State the blood parasite species.
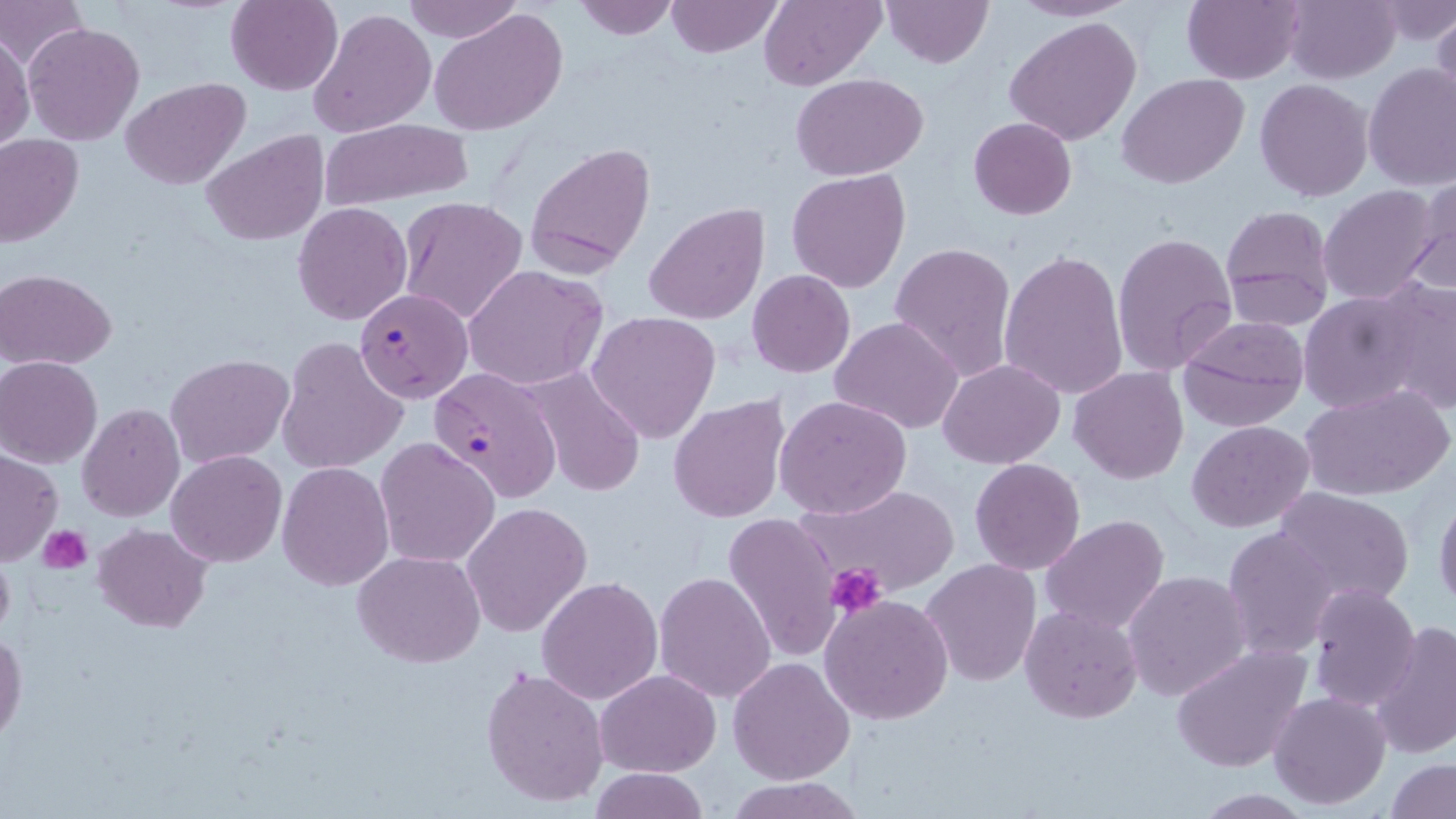

Plasmodium falciparum.

Approximate bounding boxes as (x1, y1, x2, y2) in pixels. Uninfected red blood cell locations: (1, 0, 86, 68), (226, 0, 343, 95), (402, 0, 523, 46), (572, 0, 679, 41), (665, 0, 782, 56), (758, 0, 884, 89), (881, 0, 994, 67), (1010, 0, 1139, 22), (1182, 0, 1305, 85), (1284, 0, 1400, 84), (1379, 1, 1455, 46), (308, 7, 437, 138), (431, 9, 569, 136), (1430, 11, 1456, 112), (1004, 18, 1141, 146), (23, 22, 145, 146), (1, 33, 34, 152), (1363, 64, 1456, 191), (791, 72, 930, 180), (1120, 73, 1248, 188), (121, 76, 252, 191), (1255, 80, 1373, 202), (968, 117, 1076, 220), (319, 118, 476, 208), (201, 130, 329, 245), (1, 135, 81, 244), (525, 141, 657, 275), (786, 168, 911, 293), (1410, 179, 1455, 297), (1319, 185, 1442, 306), (397, 195, 529, 326), (292, 201, 412, 325), (644, 203, 769, 324), (1220, 204, 1336, 332), (1112, 232, 1237, 376), (890, 241, 1017, 382), (999, 250, 1129, 401), (462, 265, 608, 390), (1, 269, 116, 370), (747, 269, 856, 378), (1374, 280, 1456, 415), (1297, 288, 1429, 414), (586, 311, 721, 445), (1176, 313, 1310, 431), (830, 317, 963, 435), (789, 331, 939, 492), (276, 335, 407, 474), (165, 354, 293, 467), (1, 356, 102, 468), (939, 358, 1065, 468), (1069, 367, 1189, 484), (527, 368, 645, 499), (1300, 383, 1454, 502), (668, 393, 790, 524), (776, 395, 913, 518), (78, 404, 185, 522), (1187, 421, 1313, 533), (375, 438, 500, 568), (1, 448, 62, 565), (166, 450, 287, 567), (970, 457, 1085, 574), (277, 461, 393, 589), (794, 480, 965, 595), (1273, 486, 1416, 605), (1433, 491, 1455, 614), (463, 501, 592, 637), (723, 513, 843, 663), (1041, 515, 1168, 636), (94, 524, 211, 632), (1223, 525, 1341, 662), (354, 550, 485, 668), (920, 558, 1042, 687), (654, 570, 777, 702), (1125, 570, 1251, 702), (536, 575, 663, 705), (1306, 583, 1422, 711), (819, 595, 953, 724), (1020, 604, 1143, 723), (1370, 622, 1456, 758), (0, 629, 25, 745), (1171, 642, 1313, 774), (729, 658, 856, 784), (481, 667, 609, 808), (596, 668, 720, 776), (1269, 691, 1392, 810), (1385, 756, 1455, 818), (588, 767, 708, 819), (723, 775, 865, 818). Platelet locations: (40, 527, 92, 574), (827, 563, 888, 615). Plasmodium falciparum-infected red blood cell locations: (355, 288, 473, 402), (428, 368, 565, 503). 1000x magnification. Thin blood film. One field of a larger specimen. May-Grünwald-Giemsa-stained preparation. Image is 1456×819 pixels. Light microscopy.